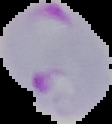
Image is 112×124 pixels. Malaria status: parasitized. The area outside the segmented cell region is set to black. From a thin blood film.